Classify this cell by malaria status.
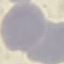
It is uninfected.

Summary:
  - Image type: cell patch, automatically extracted from a larger field of view and resized to 64 × 64 pixels
  - Stain: Giemsa
  - Capture: smartphone camera at the microscope eyepiece
  - Preparation: thin blood smear